Locate every Plasmodium parasite.
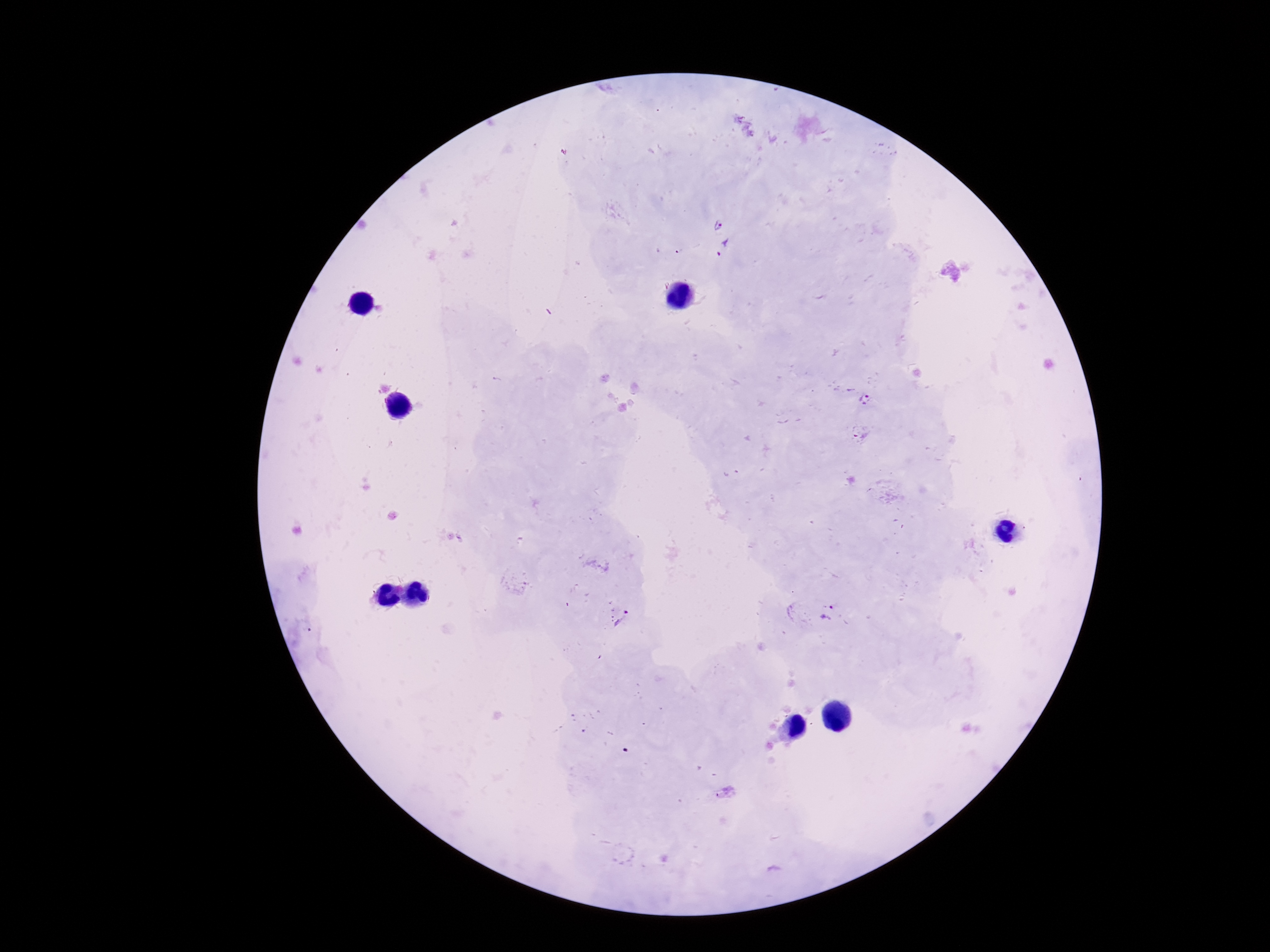

Approximate object centers, in pixels from the top-left corner.
Plasmodium parasites: (x=716, y=224), (x=725, y=250), (x=865, y=398), (x=860, y=432), (x=827, y=612), (x=619, y=616), (x=726, y=793).

Smartphone photograph taken through the microscope eyepiece. Giemsa stain. Image is 1270×952 pixels. Thick peripheral-blood smear. 100x magnification. Patient malaria status: infected. One field from this slide.